Evaluate for malaria.
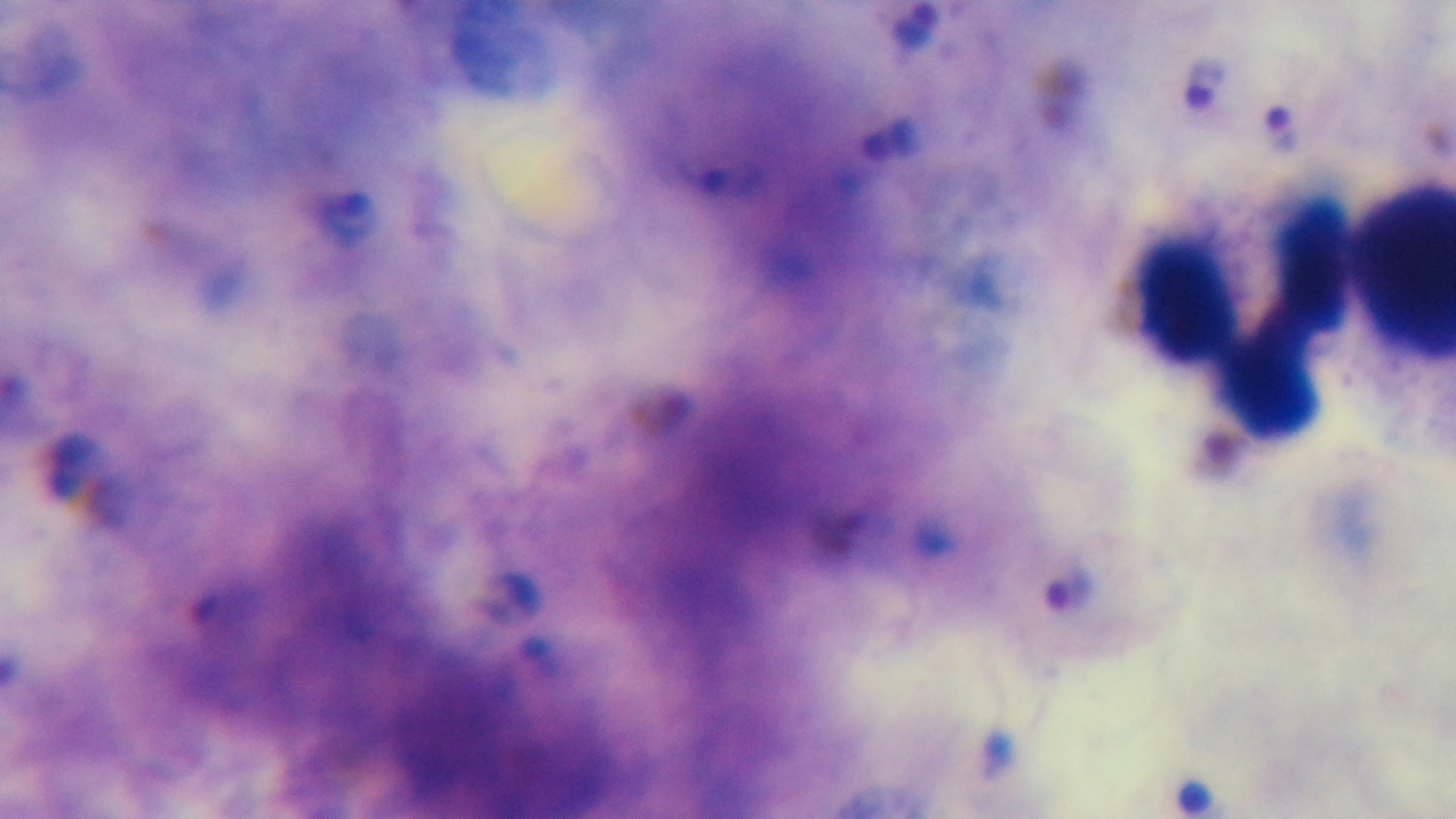

Positive.

Summary:
  - Field of view: one from the slide
  - Objective: 100x oil immersion
  - Modality: light microscopy
  - Capture: mounted 4K digital camera
  - Preparation: thick smear
  - Stain: Giemsa